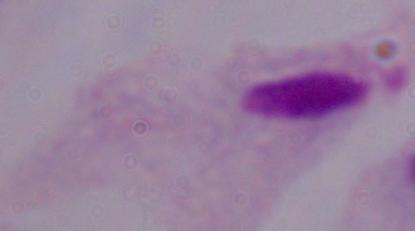 Photomicrograph. 1000x magnification. A trichomonad is seen.